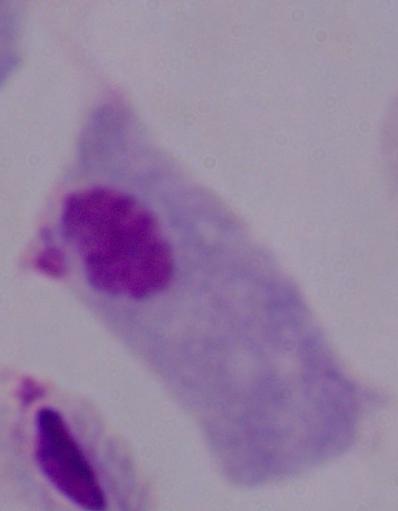
identification = trichomonad
magnification = 1000x
modality = micrograph